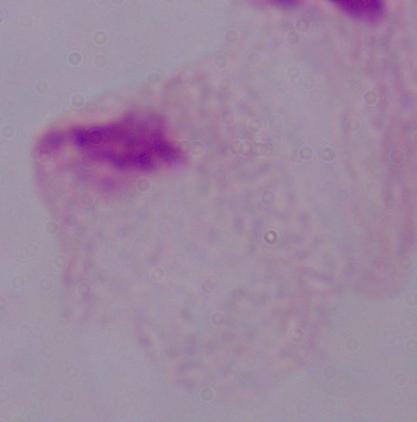

1000x magnification. Photomicrograph. A trichomonad is shown.